Locate and identify every blood parasite.
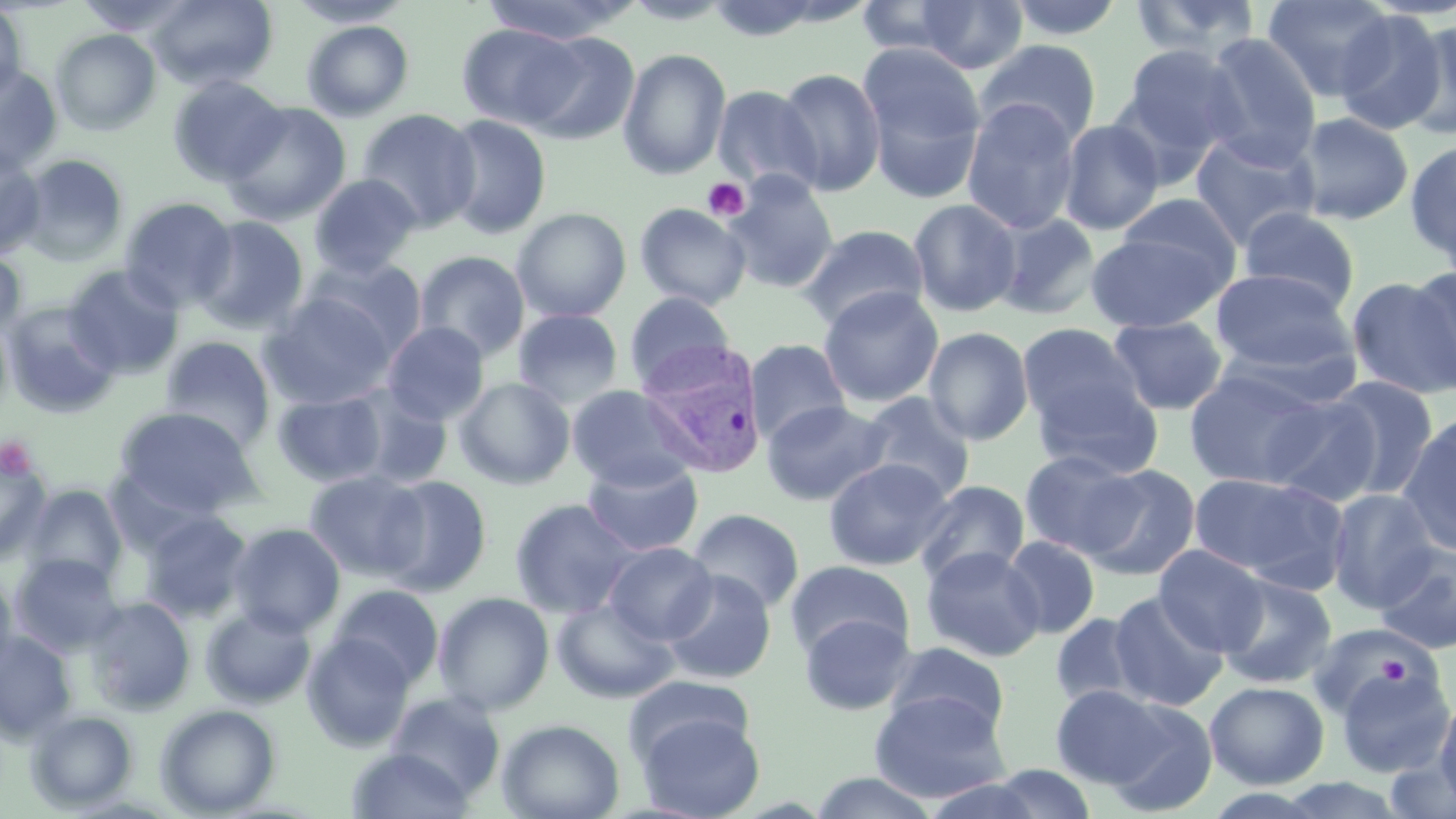

Approximate bounding boxes as named x1/y1/x2/y2 corners in pixels.
Plasmodium vivax-infected red blood cells: (x1=637, y1=340, x2=768, y2=479).
No Plasmodium falciparum, Plasmodium ovale, Plasmodium malariae, Babesia divergens, or Trypanosoma brucei observed.

Platelet locations: (x1=702, y1=177, x2=750, y2=223), (x1=0, y1=436, x2=37, y2=479), (x1=1371, y1=653, x2=1411, y2=686). Uninfected red blood cell locations: (x1=74, y1=0, x2=201, y2=36), (x1=148, y1=0, x2=278, y2=91), (x1=286, y1=0, x2=413, y2=27), (x1=478, y1=0, x2=641, y2=44), (x1=913, y1=0, x2=1028, y2=74), (x1=1004, y1=0, x2=1128, y2=42), (x1=1128, y1=0, x2=1263, y2=63), (x1=1262, y1=0, x2=1396, y2=102), (x1=0, y1=3, x2=28, y2=102), (x1=1334, y1=10, x2=1448, y2=135), (x1=1403, y1=19, x2=1456, y2=139), (x1=301, y1=20, x2=415, y2=121), (x1=456, y1=24, x2=587, y2=131), (x1=51, y1=28, x2=161, y2=136), (x1=517, y1=31, x2=640, y2=144), (x1=1200, y1=33, x2=1323, y2=165), (x1=973, y1=39, x2=1102, y2=149), (x1=857, y1=41, x2=988, y2=201), (x1=1118, y1=43, x2=1244, y2=167), (x1=618, y1=48, x2=732, y2=180), (x1=0, y1=63, x2=63, y2=175), (x1=774, y1=66, x2=887, y2=197), (x1=167, y1=75, x2=287, y2=186), (x1=712, y1=85, x2=823, y2=196), (x1=960, y1=98, x2=1082, y2=234), (x1=222, y1=101, x2=351, y2=226), (x1=357, y1=108, x2=481, y2=233), (x1=1296, y1=111, x2=1414, y2=225), (x1=442, y1=114, x2=552, y2=240), (x1=1058, y1=118, x2=1166, y2=236), (x1=1190, y1=131, x2=1320, y2=249), (x1=1404, y1=139, x2=1456, y2=266), (x1=0, y1=149, x2=46, y2=259), (x1=19, y1=154, x2=130, y2=265), (x1=309, y1=174, x2=421, y2=278), (x1=720, y1=174, x2=841, y2=294), (x1=1114, y1=193, x2=1242, y2=284), (x1=119, y1=197, x2=238, y2=312), (x1=908, y1=198, x2=1022, y2=317), (x1=634, y1=203, x2=752, y2=310), (x1=1238, y1=206, x2=1360, y2=311), (x1=512, y1=207, x2=631, y2=322), (x1=992, y1=213, x2=1101, y2=320), (x1=192, y1=216, x2=310, y2=335), (x1=796, y1=224, x2=929, y2=329), (x1=1085, y1=230, x2=1229, y2=332), (x1=414, y1=250, x2=530, y2=362), (x1=0, y1=251, x2=26, y2=340), (x1=306, y1=258, x2=428, y2=361), (x1=63, y1=265, x2=184, y2=379), (x1=1210, y1=268, x2=1355, y2=376), (x1=1409, y1=268, x2=1456, y2=390), (x1=1347, y1=276, x2=1456, y2=399), (x1=818, y1=287, x2=944, y2=408), (x1=623, y1=291, x2=737, y2=390), (x1=261, y1=292, x2=398, y2=409), (x1=3, y1=301, x2=121, y2=417), (x1=512, y1=309, x2=624, y2=408), (x1=1108, y1=316, x2=1229, y2=415), (x1=381, y1=322, x2=490, y2=426), (x1=1018, y1=323, x2=1145, y2=438), (x1=923, y1=326, x2=1034, y2=445), (x1=160, y1=336, x2=276, y2=450), (x1=745, y1=339, x2=851, y2=446), (x1=1185, y1=366, x2=1329, y2=488), (x1=1030, y1=376, x2=1165, y2=480), (x1=1324, y1=376, x2=1440, y2=500), (x1=454, y1=377, x2=576, y2=490), (x1=566, y1=385, x2=698, y2=492), (x1=346, y1=386, x2=453, y2=489), (x1=273, y1=390, x2=387, y2=487), (x1=859, y1=392, x2=977, y2=502), (x1=1262, y1=395, x2=1382, y2=507), (x1=760, y1=400, x2=893, y2=506), (x1=114, y1=406, x2=265, y2=519), (x1=1398, y1=415, x2=1456, y2=555), (x1=0, y1=449, x2=52, y2=564), (x1=1019, y1=449, x2=1143, y2=558), (x1=582, y1=458, x2=704, y2=557), (x1=824, y1=458, x2=954, y2=570), (x1=1079, y1=464, x2=1201, y2=580), (x1=304, y1=470, x2=429, y2=582), (x1=1189, y1=472, x2=1347, y2=589), (x1=376, y1=475, x2=493, y2=596), (x1=913, y1=479, x2=1030, y2=586), (x1=24, y1=485, x2=127, y2=588), (x1=1326, y1=489, x2=1441, y2=611), (x1=510, y1=497, x2=640, y2=618), (x1=687, y1=508, x2=805, y2=614), (x1=140, y1=511, x2=253, y2=622), (x1=228, y1=522, x2=346, y2=636), (x1=1002, y1=535, x2=1101, y2=639), (x1=603, y1=542, x2=717, y2=645), (x1=1374, y1=544, x2=1456, y2=655), (x1=1154, y1=545, x2=1268, y2=654), (x1=921, y1=546, x2=1046, y2=662), (x1=10, y1=553, x2=124, y2=655), (x1=784, y1=560, x2=915, y2=661), (x1=0, y1=568, x2=17, y2=681), (x1=661, y1=570, x2=776, y2=684), (x1=1216, y1=574, x2=1337, y2=689), (x1=329, y1=584, x2=444, y2=690), (x1=432, y1=591, x2=555, y2=715), (x1=1108, y1=591, x2=1228, y2=711), (x1=83, y1=597, x2=196, y2=715), (x1=551, y1=597, x2=678, y2=704), (x1=202, y1=605, x2=316, y2=709), (x1=799, y1=612, x2=916, y2=716), (x1=1050, y1=612, x2=1149, y2=709), (x1=1306, y1=622, x2=1432, y2=721), (x1=0, y1=631, x2=77, y2=743), (x1=302, y1=634, x2=415, y2=752), (x1=883, y1=642, x2=1010, y2=740), (x1=1334, y1=663, x2=1454, y2=778), (x1=623, y1=674, x2=754, y2=769), (x1=1204, y1=681, x2=1329, y2=788), (x1=1050, y1=684, x2=1169, y2=787), (x1=869, y1=691, x2=1012, y2=803), (x1=386, y1=692, x2=506, y2=801), (x1=1435, y1=693, x2=1456, y2=811), (x1=1103, y1=698, x2=1219, y2=814), (x1=155, y1=704, x2=281, y2=817), (x1=635, y1=709, x2=765, y2=819), (x1=25, y1=710, x2=138, y2=811), (x1=496, y1=718, x2=625, y2=819), (x1=346, y1=747, x2=473, y2=818), (x1=1386, y1=754, x2=1456, y2=819), (x1=982, y1=764, x2=1099, y2=819), (x1=808, y1=771, x2=942, y2=818). Slide-level diagnosis: Plasmodium vivax. May-Grünwald-Giemsa stain. 1000x magnification. Single field of view. Image is 1456×819 pixels. Thin blood smear. Light microscopy.